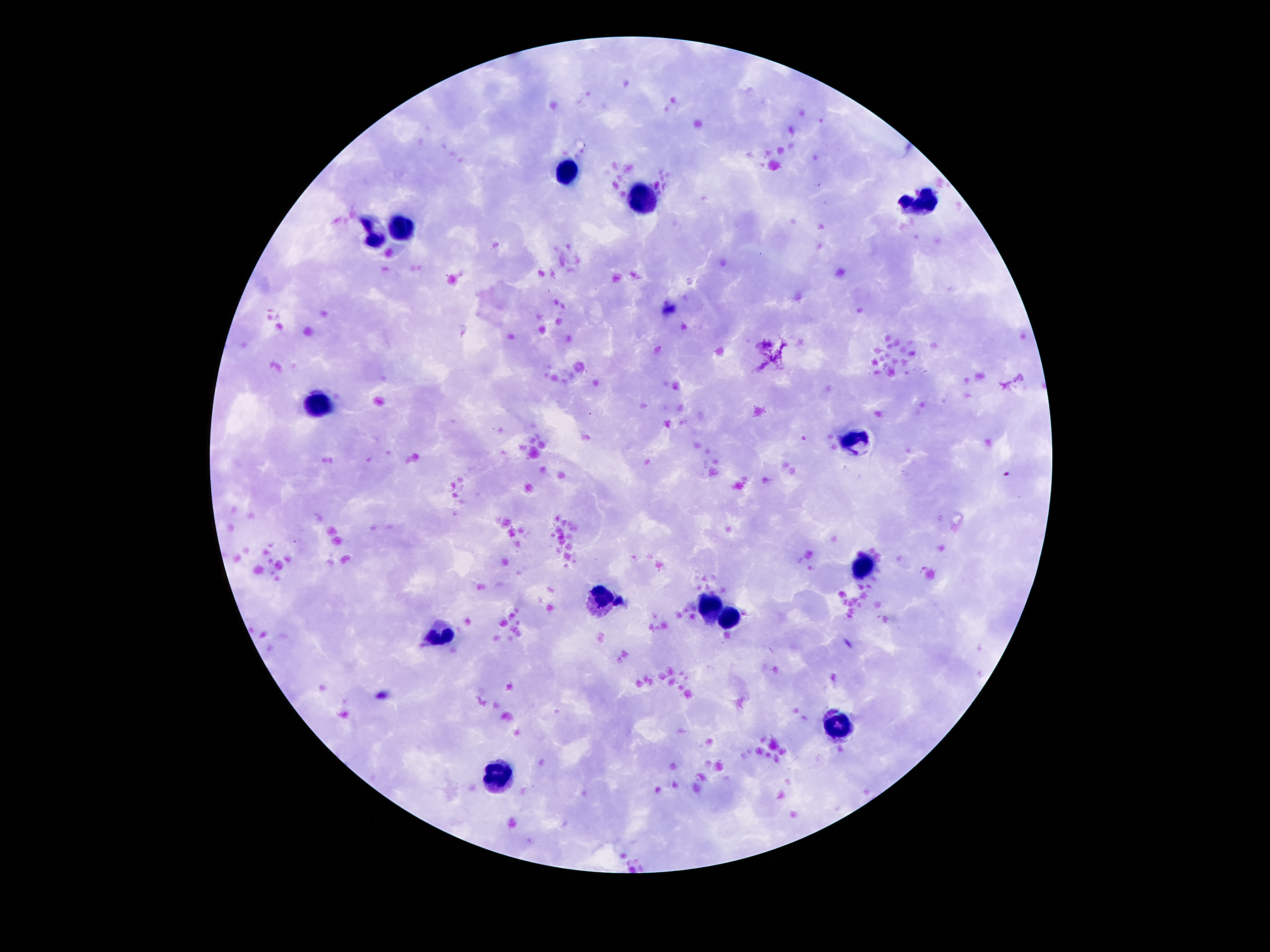
field of view = single
patient malaria status = uninfected
leukocyte locations = approximate centers as {x, y} in pixels: {569, 172}, {640, 198}, {927, 202}, {405, 226}, {371, 233}, {319, 403}, {855, 437}, {862, 566}, {601, 599}, {709, 609}, {733, 618}, {440, 635}, {836, 726}, {491, 777}
magnification = 100x
preparation = thick blood smear
image size = 1270×952 pixels
capture = smartphone camera through the microscope eyepiece
stain = Giemsa